Give the position of every malaria parasite.
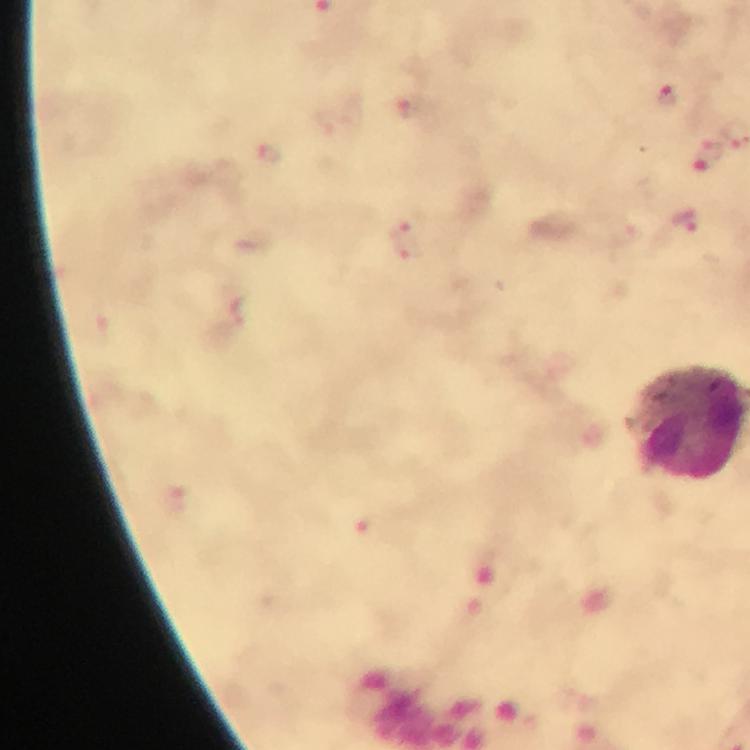
Approximate centers as (x, y) in pixels.
Malaria parasites: (669, 98), (410, 111), (707, 154), (268, 155), (685, 221).

stain: Giemsa
cropped_from: a single field of view
image_size: 750×750 pixels
immersion_oil: applied
context: from a malaria diagnostic workup
preparation: thick blood film
magnification: 100x
capture: smartphone photograph through a microscope